Outline each blood parasite and name the species.
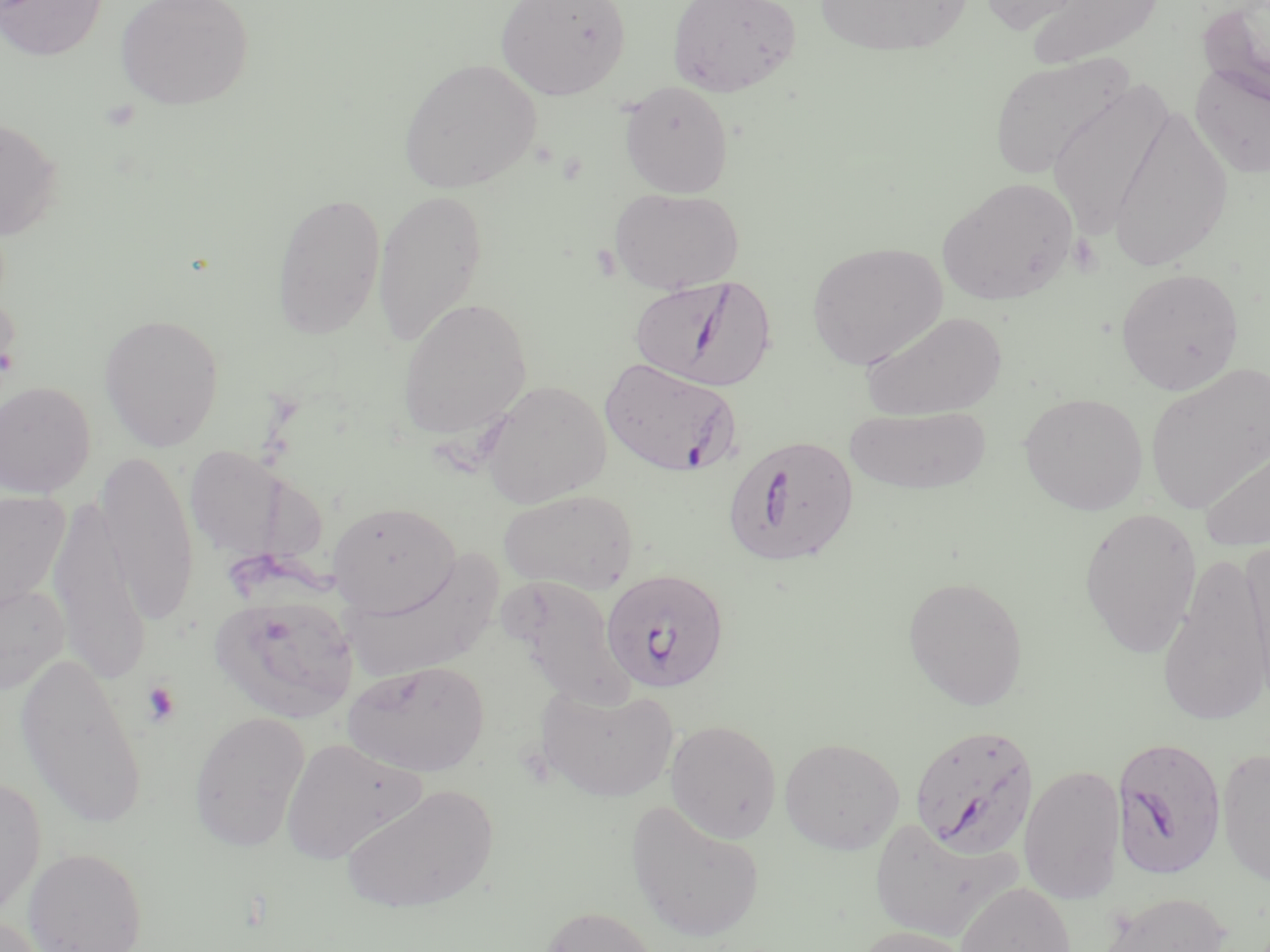

Approximate bounding boxes as [x1, y1, x2, y2] in pixels.
Plasmodium falciparum-infected red blood cells: [630, 276, 775, 391], [598, 357, 741, 478], [723, 433, 858, 567], [601, 568, 729, 694], [909, 724, 1039, 858], [1111, 735, 1227, 879].
No Plasmodium ovale, Plasmodium malariae, Plasmodium vivax, Babesia divergens, or Trypanosoma brucei observed.

{
  "slide_level_diagnosis": "Plasmodium falciparum",
  "image_size": "1270×952 pixels",
  "magnification": "1000x",
  "stain": "May-Grünwald-Giemsa",
  "modality": "light microscopy",
  "field_of_view": "one of a larger specimen",
  "uninfected_red_blood_cell_locations": "approximate bounding boxes as [x1, y1, x2, y2] in pixels: [0, 0, 108, 61], [115, 0, 254, 110], [495, 0, 631, 99], [667, 0, 802, 96], [813, 0, 975, 58], [976, 0, 1087, 34], [1025, 0, 1165, 70], [1199, 1, 1270, 107], [989, 52, 1134, 180], [398, 57, 543, 193], [1190, 63, 1270, 179], [619, 81, 734, 197], [1047, 81, 1174, 237], [1105, 103, 1235, 272], [0, 116, 64, 242], [937, 177, 1079, 306], [609, 187, 744, 294], [373, 189, 488, 347], [272, 191, 386, 339], [806, 241, 948, 370], [1114, 267, 1244, 395], [0, 290, 22, 401], [396, 297, 532, 441], [861, 310, 1008, 419], [99, 313, 225, 451], [1144, 363, 1270, 514], [478, 379, 612, 506], [0, 380, 96, 498], [1018, 392, 1149, 515], [844, 405, 992, 495], [1199, 434, 1270, 555], [185, 445, 290, 560], [96, 449, 200, 624], [497, 488, 639, 593], [0, 490, 70, 621], [48, 498, 150, 684], [327, 502, 461, 616], [1079, 505, 1203, 657], [1239, 537, 1270, 707], [343, 550, 504, 686], [1157, 554, 1270, 728], [501, 573, 636, 710], [903, 575, 1029, 710], [0, 578, 70, 697], [210, 593, 359, 722], [15, 651, 148, 830], [342, 660, 489, 777], [534, 680, 679, 803], [189, 710, 310, 852], [665, 719, 782, 842], [280, 735, 422, 865], [779, 736, 905, 855], [1216, 747, 1270, 886], [1019, 763, 1126, 905], [0, 776, 47, 922], [342, 783, 499, 915], [625, 799, 765, 944], [870, 817, 1019, 943], [22, 847, 149, 952], [955, 881, 1076, 952], [1098, 891, 1234, 952], [534, 905, 665, 952], [0, 915, 54, 951], [850, 924, 980, 952]",
  "preparation": "thin blood smear",
  "platelet_locations": "approximate bounding boxes as [x1, y1, x2, y2] in pixels: [1068, 233, 1103, 276], [141, 680, 181, 726]"
}